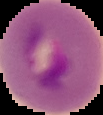
Summary:
  - Image type: segmented cell region with the area outside set to black
  - Malaria status: parasitized
  - Image size: 103×115 pixels
  - Preparation: thin blood film